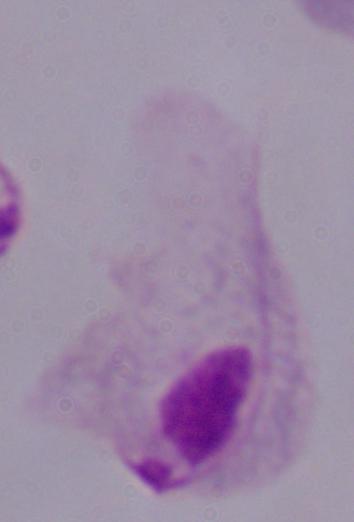

modality = micrograph
identification = trichomonad
magnification = 1000x